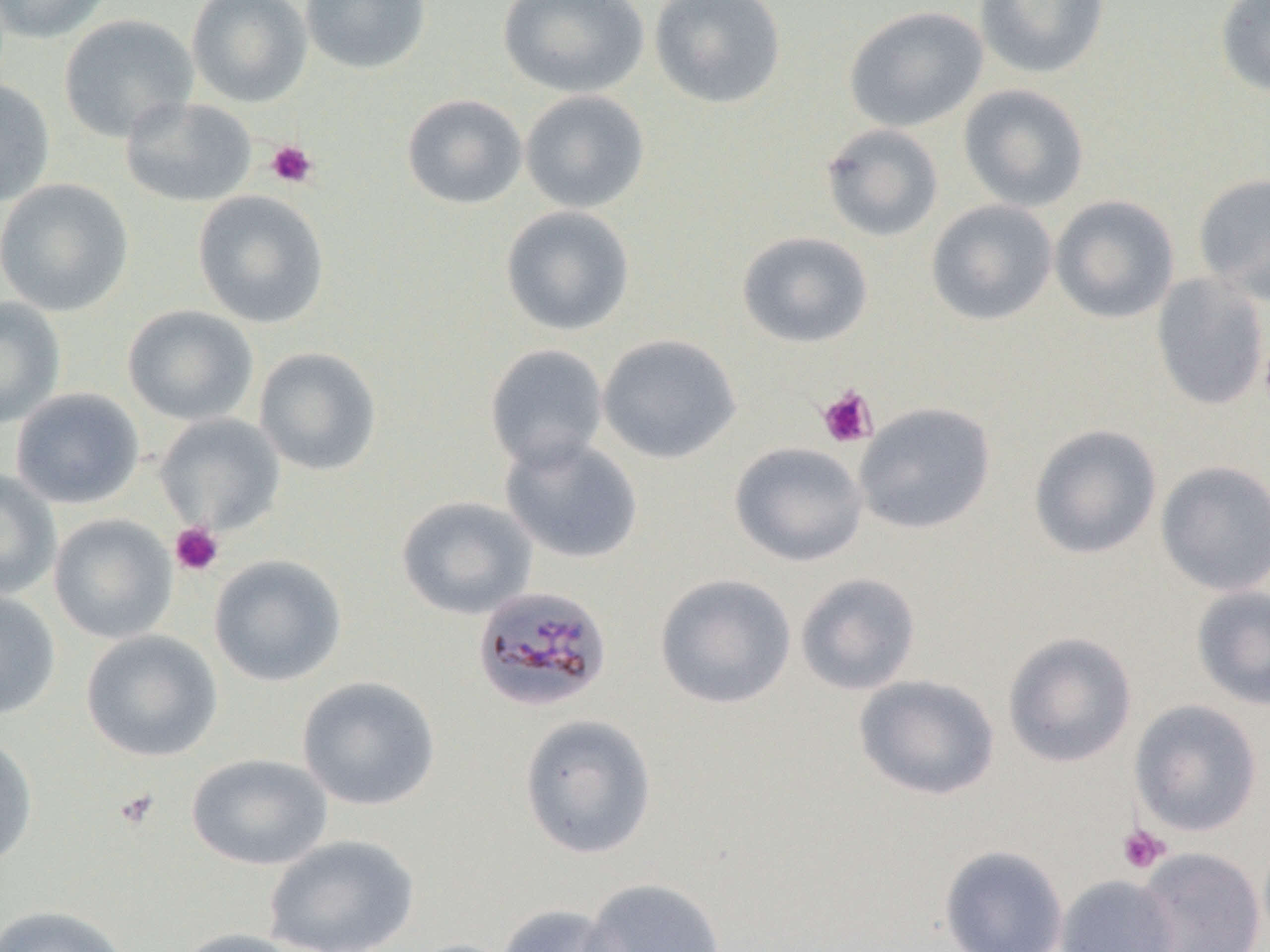

Summary:
  - Coordinate format: approximate bounding boxes as (x1, y1, x2, y2) in pixels
  - Platelet locations: (265, 140, 319, 189), (817, 385, 878, 448), (170, 522, 224, 576), (114, 788, 159, 831), (1117, 824, 1170, 874)
  - Uninfected red blood cell locations: (0, 0, 113, 44), (186, 0, 313, 107), (300, 0, 432, 75), (497, 0, 650, 99), (649, 0, 787, 109), (974, 0, 1109, 79), (1215, 0, 1270, 98), (843, 5, 988, 132), (58, 14, 199, 143), (0, 79, 56, 207), (958, 83, 1089, 212), (520, 90, 650, 214), (402, 94, 527, 210), (119, 97, 258, 207), (820, 123, 944, 242), (1192, 173, 1270, 304), (0, 179, 134, 317), (192, 190, 330, 328), (1049, 194, 1180, 324), (926, 199, 1058, 326), (500, 205, 635, 337), (737, 231, 873, 348), (1151, 273, 1269, 411), (0, 296, 66, 428), (122, 305, 259, 425), (597, 333, 742, 464), (484, 343, 608, 471), (253, 346, 382, 476), (10, 388, 144, 509), (853, 401, 997, 535), (155, 413, 286, 534), (1028, 423, 1163, 560), (500, 434, 643, 564), (729, 441, 868, 567), (1155, 460, 1270, 596), (0, 469, 61, 600), (395, 495, 538, 620), (49, 514, 178, 644), (208, 554, 347, 687), (795, 572, 921, 695), (654, 573, 797, 710), (1191, 585, 1270, 711), (0, 589, 61, 721), (81, 629, 223, 762), (1002, 631, 1137, 768), (853, 674, 1000, 801), (296, 675, 441, 810), (1129, 699, 1263, 836), (517, 713, 658, 860), (0, 733, 38, 870), (186, 753, 333, 871), (264, 834, 419, 952), (939, 845, 1068, 952), (1134, 847, 1266, 952), (1055, 874, 1179, 952), (580, 877, 727, 952), (0, 904, 133, 952), (495, 904, 625, 952), (171, 928, 310, 952)
  - Plasmodium malariae-infected red blood cell locations: (471, 585, 613, 714)
  - Slide-level diagnosis: Plasmodium malariae
  - Image size: 1270×952 pixels
  - Preparation: thin blood smear
  - Magnification: 1000x
  - Field of view: single
  - Stain: May-Grünwald-Giemsa
  - Modality: light microscopy